Report the malaria status of this cell.
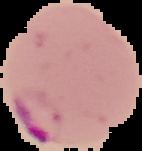
Parasitized.

Image is 142×151 pixels. From a thin blood smear. The area outside the segmented cell region is set to black.